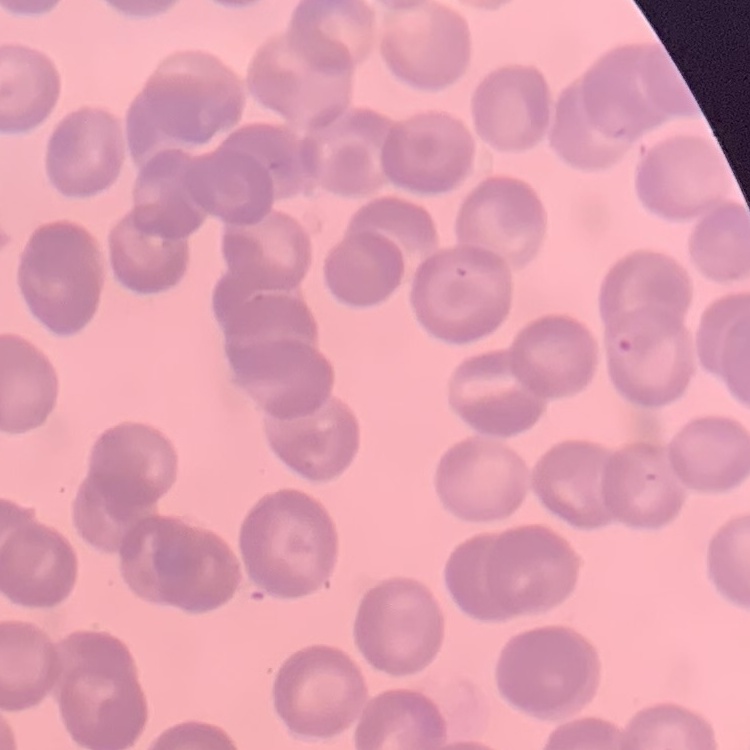
Summary:
  - Red blood cell morphology: rouleaux formation
  - Image type: square crop of a larger photomicrograph
  - Preparation: thin blood smear
  - Stain: Field's or Giemsa